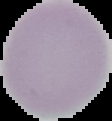

preparation: thin blood smear
result: negative for Plasmodium parasites
image_type: cell region segmented out of the field of view; surrounding area masked to black
image_size: 112×121 pixels